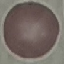

Summary:
  - Malaria status: uninfected
  - Preparation: thin blood film
  - Stain: Giemsa
  - Capture: smartphone camera at the microscope eyepiece
  - Image type: automatically extracted cell patch, resized to 64 × 64 pixels